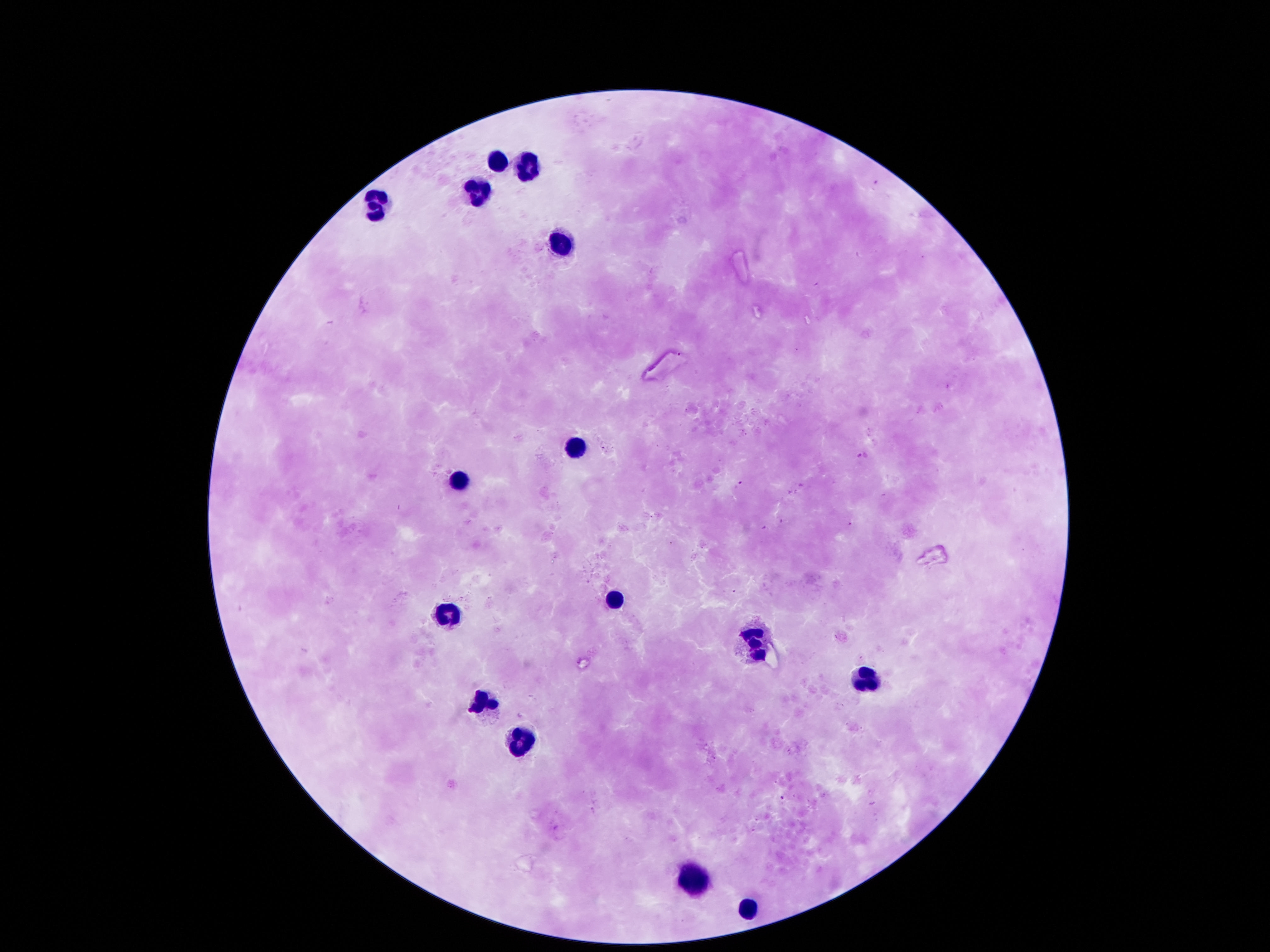

magnification: 100x
leukocyte_locations: 'approximate centers as (x, y) in pixels: (495, 155), (531, 171), (473, 186), (373, 212), (557, 249), (570, 448), (453, 481), (615, 594), (444, 620), (757, 645), (867, 675), (486, 704), (524, 742), (689, 881), (747, 907)'
field_of_view: single
patient_malaria_status: not infected
stain: Giemsa
capture: smartphone camera through the microscope eyepiece
preparation: thick blood smear
image_size: 1270×952 pixels